Report the malaria status of this cell.
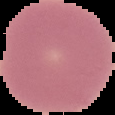

It is uninfected.

Image is 115×115 pixels. From a thin blood smear. Segmented cell region on a black background.